Outline each blood parasite and name the species.
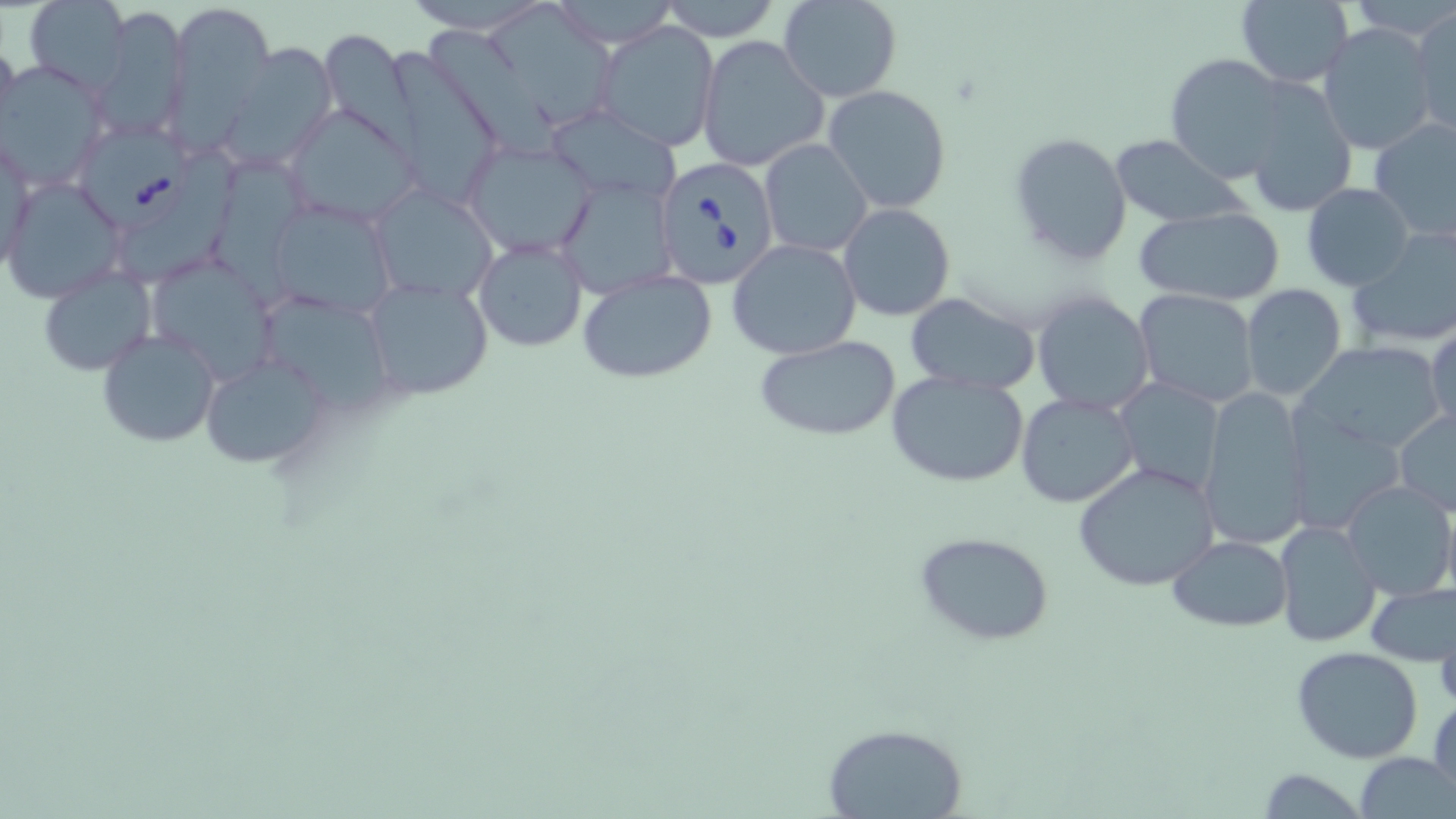
Approximate bounding boxes as (x1,y1)-(x2,y2) corner pairs in pixels.
Babesia divergens-infected red blood cells: (79,124)-(189,228), (653,154)-(782,289).
No Plasmodium falciparum, Plasmodium ovale, Plasmodium malariae, Plasmodium vivax, or Trypanosoma brucei observed.

Summary:
  - Uninfected red blood cell locations: (165,0)-(276,133), (403,0)-(556,31), (546,0)-(679,46), (779,0)-(901,102), (23,1)-(132,94), (655,1)-(784,42), (1233,1)-(1354,87), (92,4)-(188,142), (1409,6)-(1455,137), (595,22)-(719,154), (1318,22)-(1436,157), (430,33)-(559,158), (0,36)-(19,143), (696,36)-(830,172), (319,39)-(421,175), (222,40)-(335,170), (383,52)-(504,212), (1165,54)-(1290,181), (1,62)-(107,191), (1241,80)-(1359,219), (823,85)-(953,215), (286,104)-(422,226), (543,107)-(680,206), (1369,117)-(1456,242), (3,127)-(35,277), (1009,131)-(1134,267), (1109,135)-(1244,226), (463,139)-(599,258), (759,139)-(872,257), (117,151)-(238,282), (211,154)-(323,309), (556,176)-(678,299), (2,178)-(123,302), (1301,183)-(1415,292), (369,185)-(496,303), (265,197)-(398,318), (839,202)-(955,321), (1132,206)-(1288,306), (1346,228)-(1456,351), (475,237)-(589,353), (726,239)-(862,359), (146,254)-(276,382), (38,266)-(154,376), (576,270)-(717,383), (362,276)-(495,401), (1240,285)-(1349,401), (1134,290)-(1259,407), (1031,291)-(1155,416), (902,293)-(1039,394), (270,297)-(386,417), (1426,322)-(1455,434), (97,329)-(221,446), (753,336)-(904,439), (1298,341)-(1446,454), (200,353)-(332,470), (886,370)-(1031,490), (1116,378)-(1223,494), (1196,387)-(1311,551), (1015,392)-(1140,507), (1289,398)-(1405,530), (1394,407)-(1456,517), (1072,461)-(1221,592), (1339,480)-(1456,600), (1440,492)-(1456,607), (1275,520)-(1383,648), (914,531)-(1057,645), (1168,534)-(1293,633), (1366,583)-(1456,665), (1434,610)-(1456,714), (1292,646)-(1425,765), (1431,692)-(1456,805), (823,723)-(969,817), (1355,751)-(1453,818), (1254,768)-(1366,818)
  - Slide-level diagnosis: Babesia divergens
  - Preparation: thin blood smear
  - Magnification: 1000x
  - Field of view: one of a larger specimen
  - Modality: light microscopy
  - Stain: May-Grünwald-Giemsa
  - Image size: 1456×819 pixels